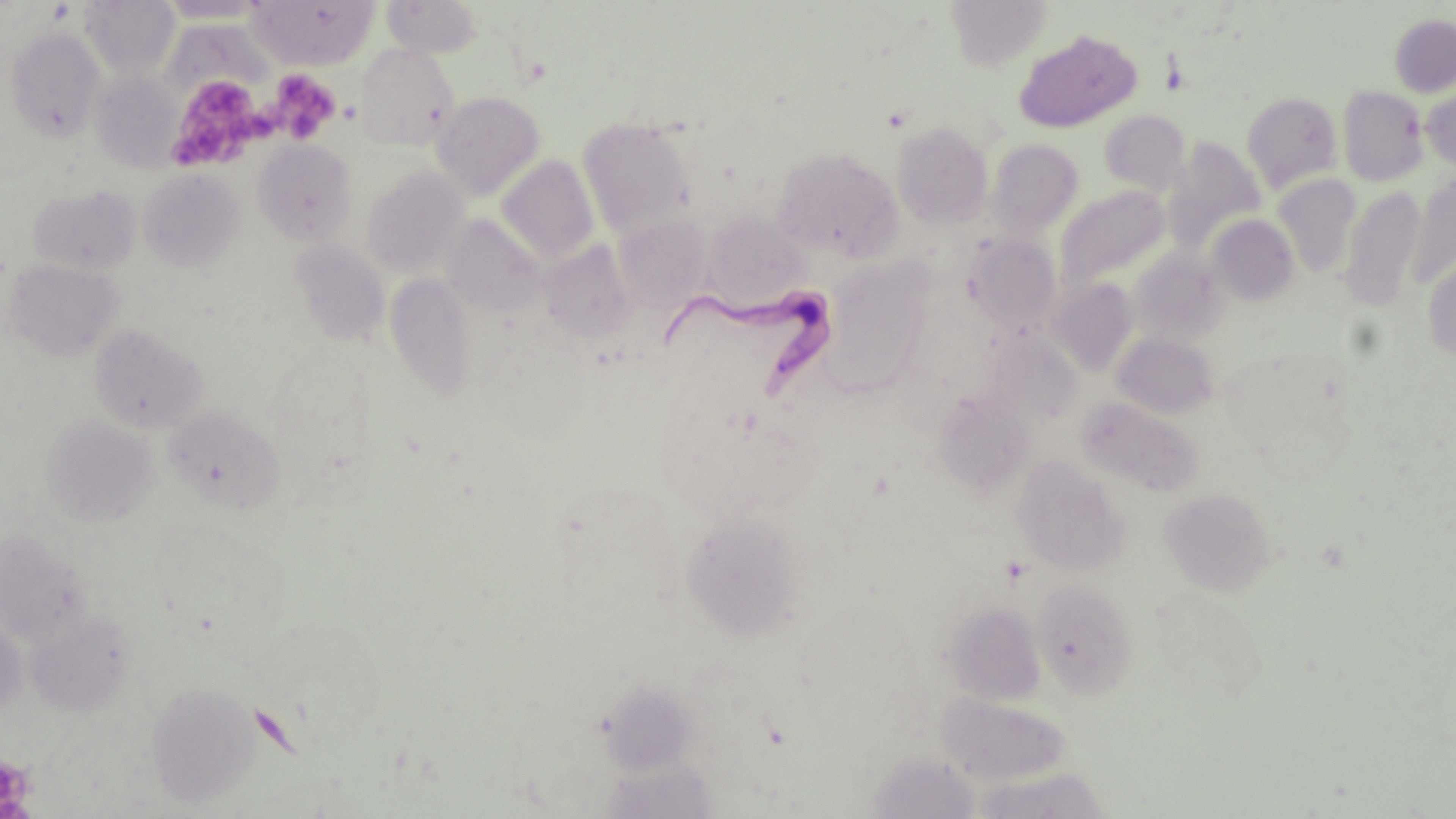

Summary:
  - Coordinate format: approximate bounding boxes as named x1/y1/x2/y2 corners in pixels
  - Trypanosoma brucei locations: (x1=665, y1=286, x2=834, y2=404)
  - Platelet locations: (x1=271, y1=70, x2=340, y2=143), (x1=166, y1=71, x2=271, y2=170), (x1=0, y1=754, x2=37, y2=815)
  - Uninfected red blood cell locations: (x1=247, y1=0, x2=378, y2=69), (x1=383, y1=0, x2=483, y2=57), (x1=946, y1=0, x2=1051, y2=71), (x1=80, y1=1, x2=180, y2=78), (x1=155, y1=1, x2=267, y2=23), (x1=1389, y1=13, x2=1456, y2=97), (x1=6, y1=27, x2=105, y2=141), (x1=1014, y1=30, x2=1141, y2=133), (x1=354, y1=42, x2=460, y2=150), (x1=90, y1=71, x2=183, y2=171), (x1=1420, y1=85, x2=1456, y2=173), (x1=1337, y1=86, x2=1429, y2=187), (x1=431, y1=91, x2=545, y2=199), (x1=1241, y1=92, x2=1343, y2=193), (x1=1100, y1=110, x2=1191, y2=194), (x1=578, y1=118, x2=697, y2=236), (x1=892, y1=121, x2=993, y2=229), (x1=252, y1=139, x2=357, y2=245), (x1=985, y1=139, x2=1083, y2=237), (x1=1165, y1=139, x2=1266, y2=252), (x1=772, y1=147, x2=903, y2=262), (x1=497, y1=155, x2=599, y2=266), (x1=362, y1=166, x2=471, y2=278), (x1=138, y1=167, x2=245, y2=273), (x1=1407, y1=173, x2=1455, y2=288), (x1=1272, y1=174, x2=1361, y2=277), (x1=28, y1=183, x2=141, y2=275), (x1=1057, y1=186, x2=1170, y2=291), (x1=1340, y1=187, x2=1427, y2=312), (x1=702, y1=213, x2=809, y2=306), (x1=1206, y1=214, x2=1300, y2=306), (x1=443, y1=215, x2=546, y2=317), (x1=614, y1=215, x2=711, y2=311), (x1=443, y1=227, x2=640, y2=326), (x1=962, y1=233, x2=1062, y2=335), (x1=289, y1=238, x2=390, y2=346), (x1=538, y1=240, x2=639, y2=342), (x1=1129, y1=247, x2=1229, y2=346), (x1=1422, y1=252, x2=1456, y2=360), (x1=3, y1=258, x2=124, y2=361), (x1=825, y1=270, x2=929, y2=407), (x1=385, y1=272, x2=477, y2=401), (x1=1049, y1=279, x2=1139, y2=375), (x1=88, y1=323, x2=208, y2=435), (x1=1112, y1=333, x2=1219, y2=419), (x1=934, y1=392, x2=1037, y2=497), (x1=1077, y1=396, x2=1204, y2=498), (x1=162, y1=404, x2=285, y2=513), (x1=40, y1=414, x2=160, y2=527), (x1=1011, y1=455, x2=1131, y2=576), (x1=1159, y1=488, x2=1275, y2=596), (x1=682, y1=513, x2=804, y2=641), (x1=0, y1=528, x2=93, y2=646), (x1=1031, y1=578, x2=1138, y2=698), (x1=942, y1=600, x2=1046, y2=706), (x1=26, y1=611, x2=136, y2=717), (x1=0, y1=616, x2=26, y2=717), (x1=601, y1=677, x2=695, y2=777), (x1=146, y1=681, x2=261, y2=810), (x1=938, y1=691, x2=1072, y2=785), (x1=867, y1=751, x2=981, y2=818), (x1=599, y1=757, x2=720, y2=819)
  - Slide-level diagnosis: Trypanosoma brucei
  - Magnification: 1000x
  - Image size: 1456×819 pixels
  - Field of view: one of a larger specimen
  - Preparation: thin blood film
  - Modality: optical microscopy
  - Stain: May-Grünwald-Giemsa